Comment on the morphology of the red blood cells.
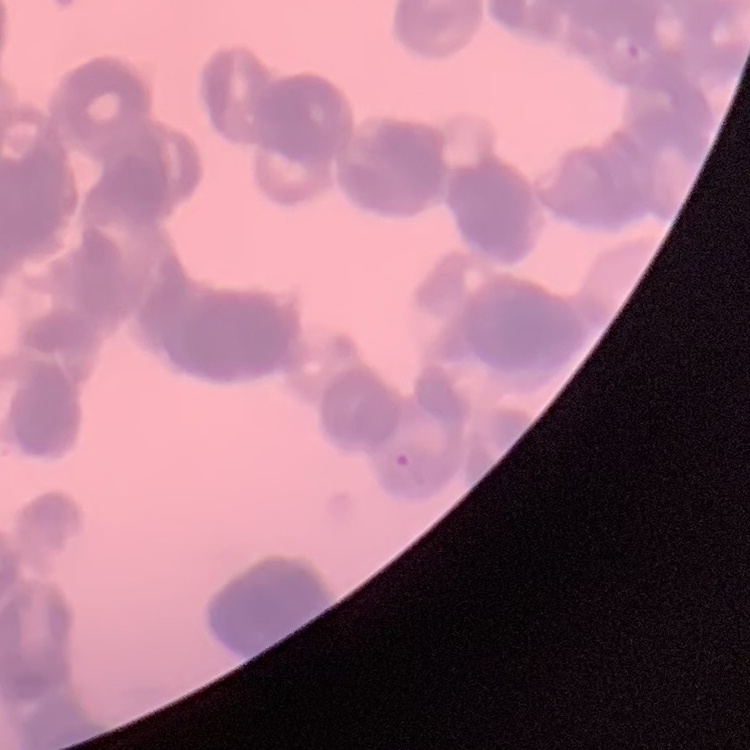

Rouleaux formation.

{
  "preparation": "thin blood film",
  "image_type": "one tile cut from a larger photomicrograph",
  "stain": "Field's or Giemsa"
}